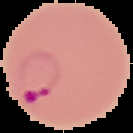
Summary:
  - Result: malaria parasites detected
  - Preparation: thin blood film
  - Image size: 133×133 pixels
  - Image type: cell region segmented out of the field of view; surrounding area masked to black